Name the parasite shown.
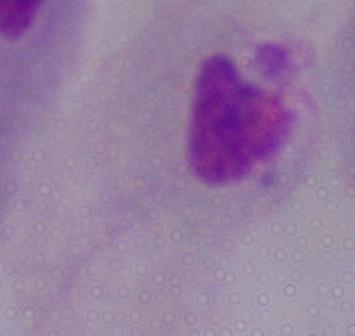
This is a trichomonad.

Summary:
  - Modality: photomicrograph
  - Magnification: 1000x